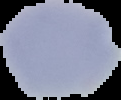

image_type: cell region segmented out of the field of view; surrounding area masked to black
result: negative for Plasmodium parasites
preparation: thin blood film
image_size: 121×100 pixels